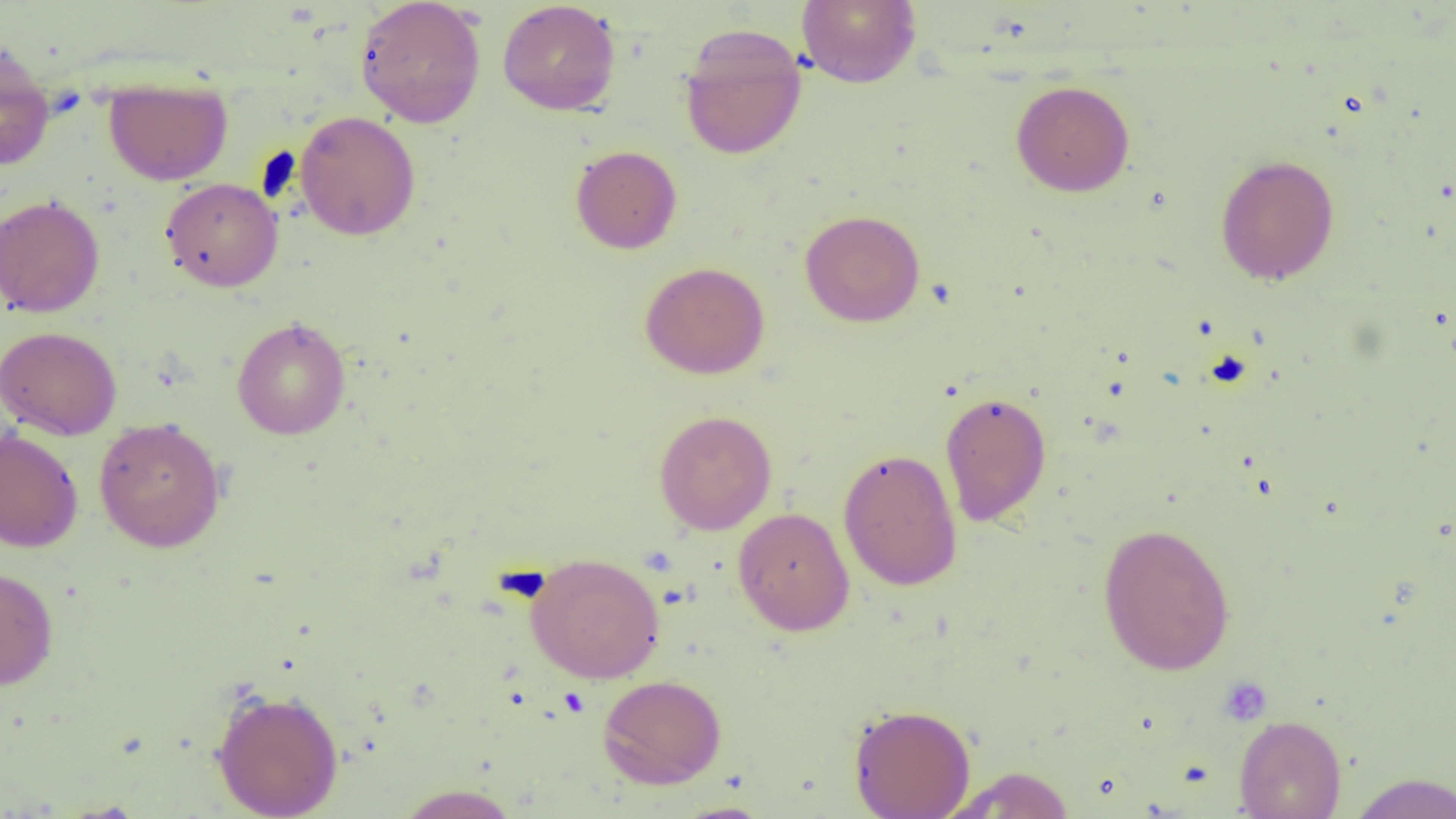
Summary:
  - Coordinate format: approximate bounding boxes as [x1, y1, x2, y2] in pixels
  - Uninfected red blood cell locations: [355, 0, 486, 128], [796, 0, 921, 88], [497, 1, 621, 115], [679, 25, 808, 161], [0, 44, 55, 171], [103, 77, 232, 185], [1011, 79, 1135, 197], [295, 111, 421, 241], [570, 145, 682, 254], [1215, 154, 1340, 286], [161, 177, 283, 292], [0, 194, 105, 318], [799, 210, 925, 327], [640, 261, 770, 379], [231, 316, 350, 440], [0, 325, 122, 440], [939, 391, 1052, 526], [654, 410, 777, 534], [94, 417, 226, 553], [0, 428, 83, 552], [838, 448, 962, 590], [733, 507, 854, 635], [1097, 522, 1236, 675], [526, 553, 665, 683], [0, 567, 58, 690], [598, 674, 727, 789], [211, 686, 345, 819], [848, 703, 976, 818], [1233, 714, 1347, 819], [946, 766, 1077, 818], [1347, 772, 1456, 818], [394, 784, 521, 818], [668, 801, 778, 819]
  - Platelet locations: [1217, 676, 1273, 725]
  - Slide-level diagnosis: negative for blood parasites
  - Magnification: 1000x
  - Image size: 1456×819 pixels
  - Field of view: single
  - Preparation: thin blood smear
  - Modality: optical microscopy